Report the malaria status of this cell.
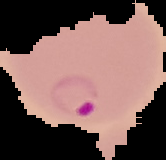

Parasitized.

image size = 166×160 pixels
preparation = thin blood smear
image type = segmented cell region with the area outside set to black